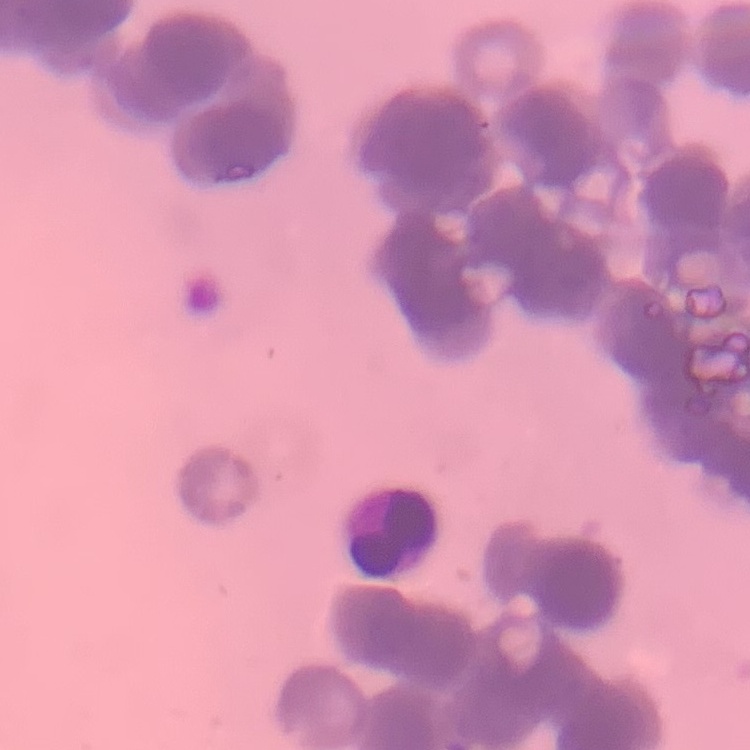

Summary:
  - Red blood cell morphology: rouleaux formation
  - Stain: Field's or Giemsa
  - Image type: one tile cut from a larger photomicrograph
  - Preparation: thin blood film